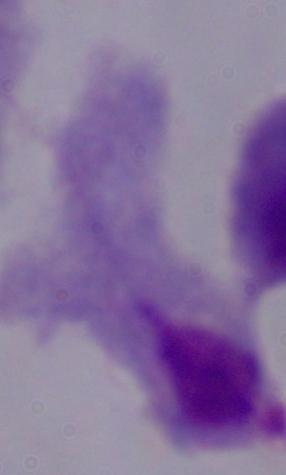
{
  "identification": "trichomonad",
  "modality": "photomicrograph",
  "magnification": "1000x"
}